Locate every Plasmodium parasite.
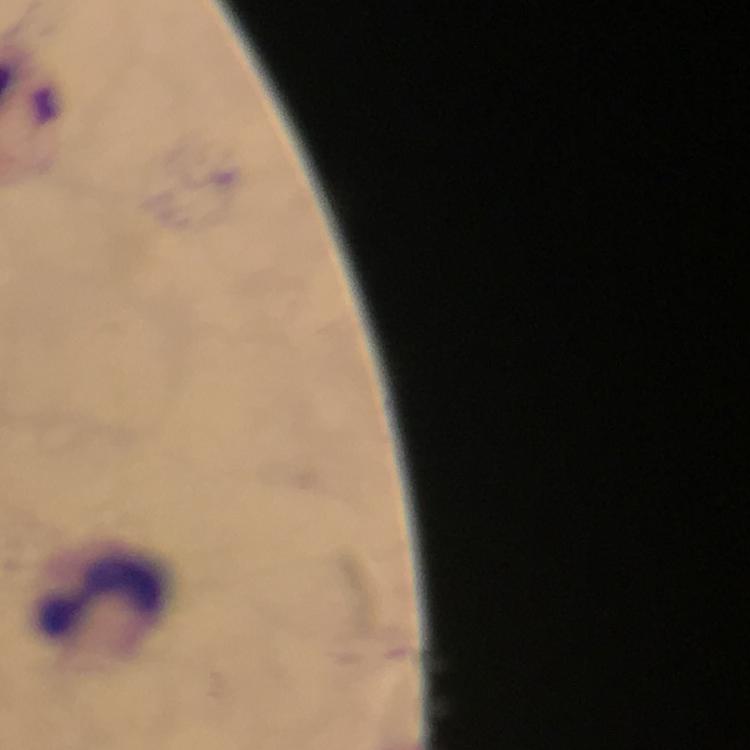

No Plasmodium parasites detected.

Approximate centers as (x, y) in pixels. Leukocyte locations: (101, 600). At 100x magnification. Cropped region of a single field of view. Thick blood smear. Smartphone photograph taken through a microscope. Immersion oil was used. Giemsa stain. Image is 750×750 pixels. From a malaria diagnostic workup.